Locate Plasmodium parasites and leukocytes.
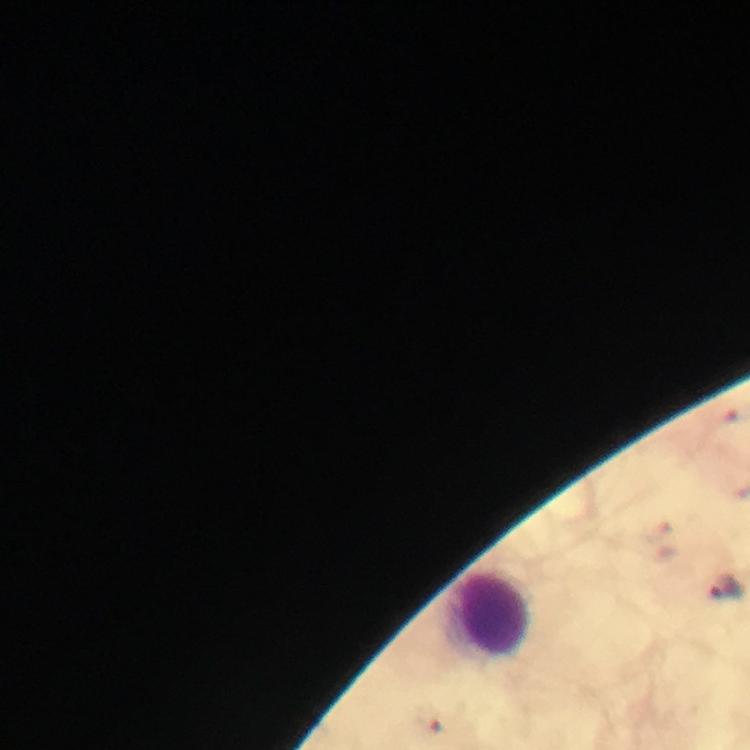
Approximate centers as {x, y} in pixels.
Plasmodium parasites: {725, 589}, {431, 722}.
Leukocytes: {490, 614}.

Giemsa-stained preparation. From a diagnostic examination for malaria. 100x magnification. Image is 750×750 pixels. Cropped region of a single field of view. Smartphone photograph taken through a microscope. Thick smear. Immersion oil applied.